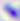
Toxoplasma gondii is seen. Micrograph. Captured at 400x magnification.